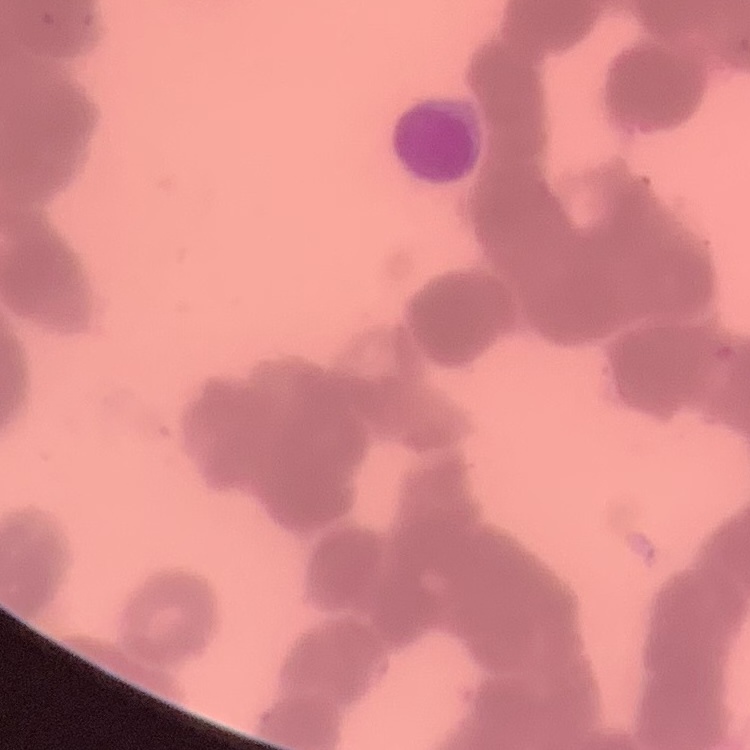

The red blood cells show rouleaux formation. Field's or Giemsa stain. One tile cut from a larger photomicrograph. Thin blood film.